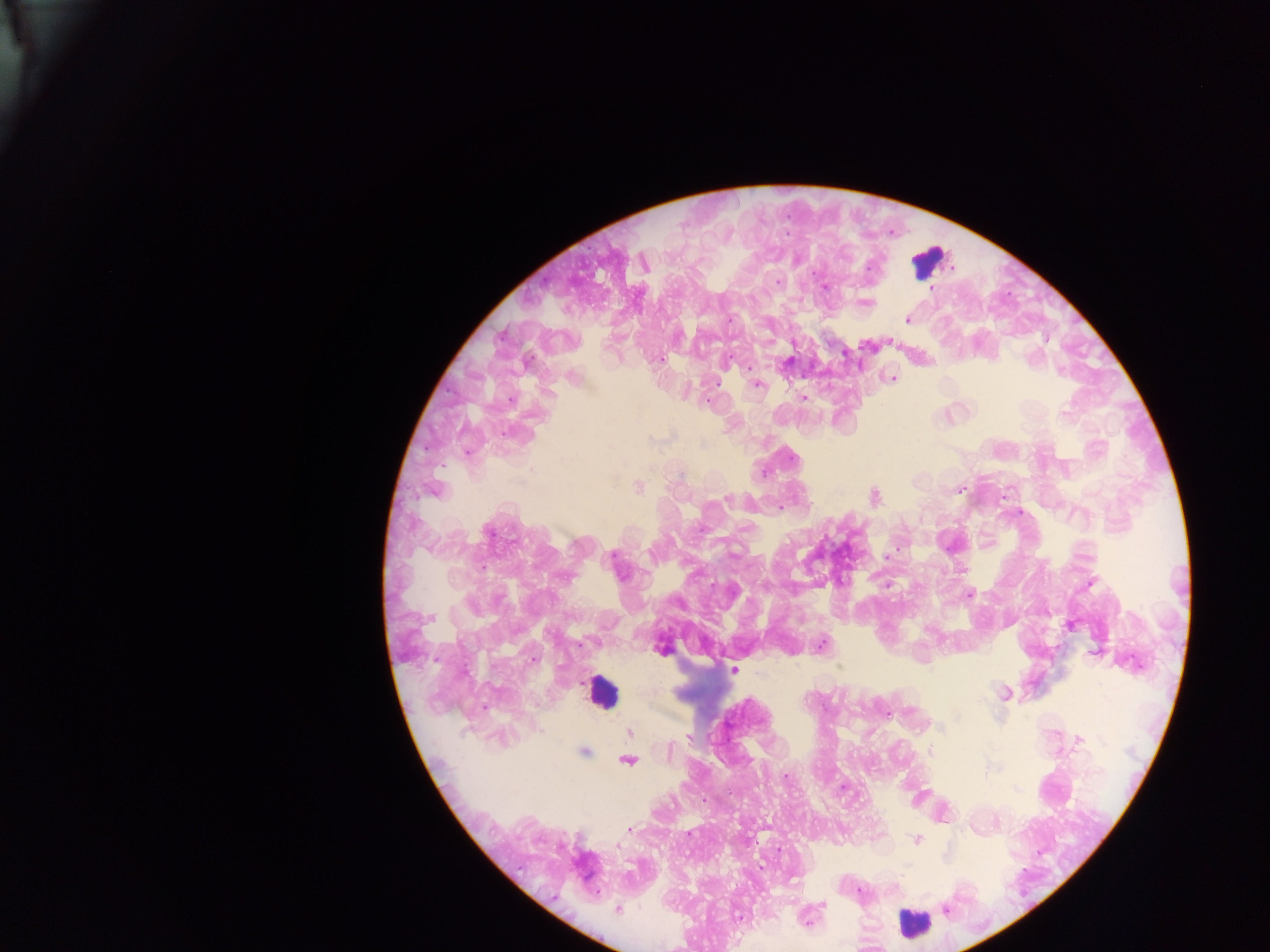
Approximate centers as x y in pixels. Malaria parasite locations: 869 266; 777 282; 825 287; 932 288; 867 303; 729 319; 906 319; 659 359; 786 363; 747 367; 892 379; 758 385; 803 398; 709 399; 1065 413; 508 434; 702 443; 532 470; 638 487; 959 490; 434 492; 875 497; 727 499; 780 508; 1021 513; 488 532; 612 555; 887 556; 482 567; 963 570; 1090 583; 969 595; 430 618; 1070 626; 822 644; 661 650; 1095 652; 532 659; 734 670; 1004 694; 885 713; 940 728; 630 732; 689 737; 1080 739; 668 750; 584 752; 930 752; 628 761; 786 777; 630 829; 917 840; 617 846; 860 891; 822 906; 617 910; 945 910; 739 918; 805 920. Leukocyte locations: 929 260; 601 692; 912 923. Photographed through a microscope with a mobile-phone camera. Thick blood film. One field of view. Sample from Ghana. Image is 1270×952 pixels.